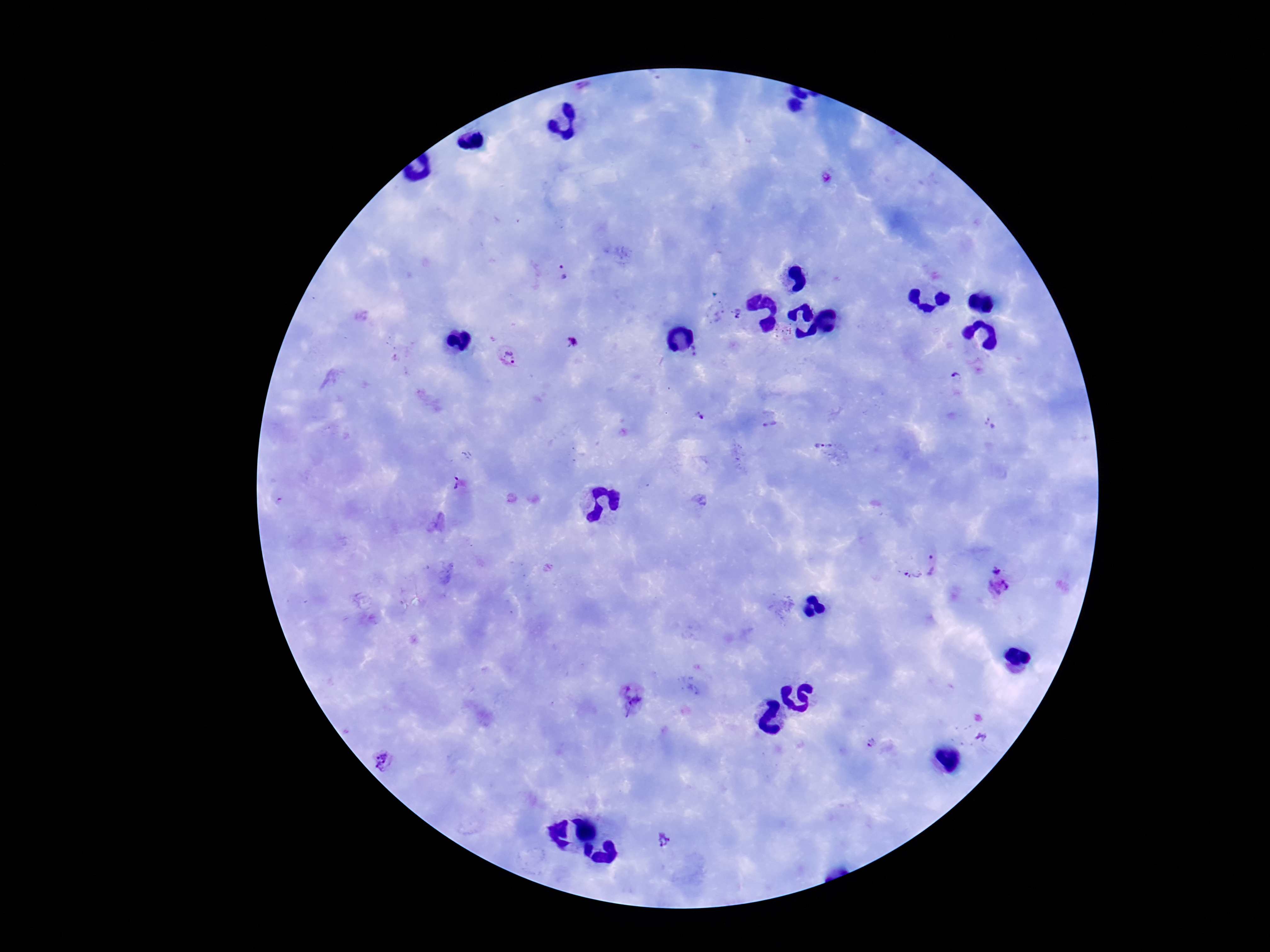

{
  "plasmodium_parasite_locations": "approximate centers as [x, y] in pixels: [824, 180], [561, 272], [738, 315], [571, 343], [695, 352], [507, 358], [957, 377], [701, 415], [989, 424], [768, 425], [816, 444], [456, 484], [936, 566], [995, 567], [911, 578], [999, 587], [630, 702], [981, 737], [870, 745], [383, 761], [662, 841]",
  "stain": "Giemsa",
  "field_of_view": "single",
  "capture": "smartphone camera through the microscope eyepiece",
  "preparation": "thick blood smear",
  "image_size": "1270×952 pixels",
  "patient_malaria_status": "positive",
  "magnification": "100x"
}